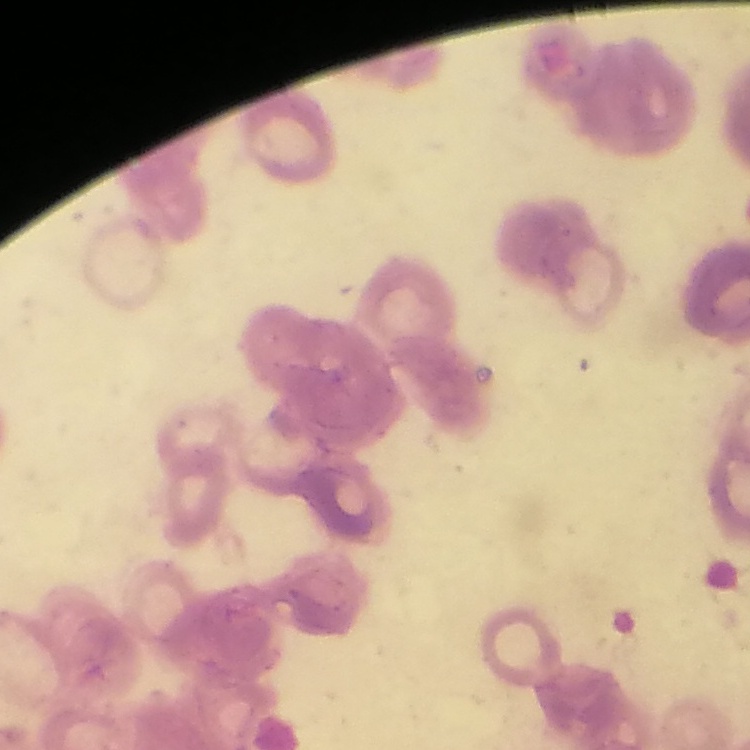

Summary:
  - Erythrocyte morphology: rouleaux formation
  - Image type: one tile cut from a larger photomicrograph
  - Preparation: thin peripheral smear
  - Stain: Field's or Giemsa